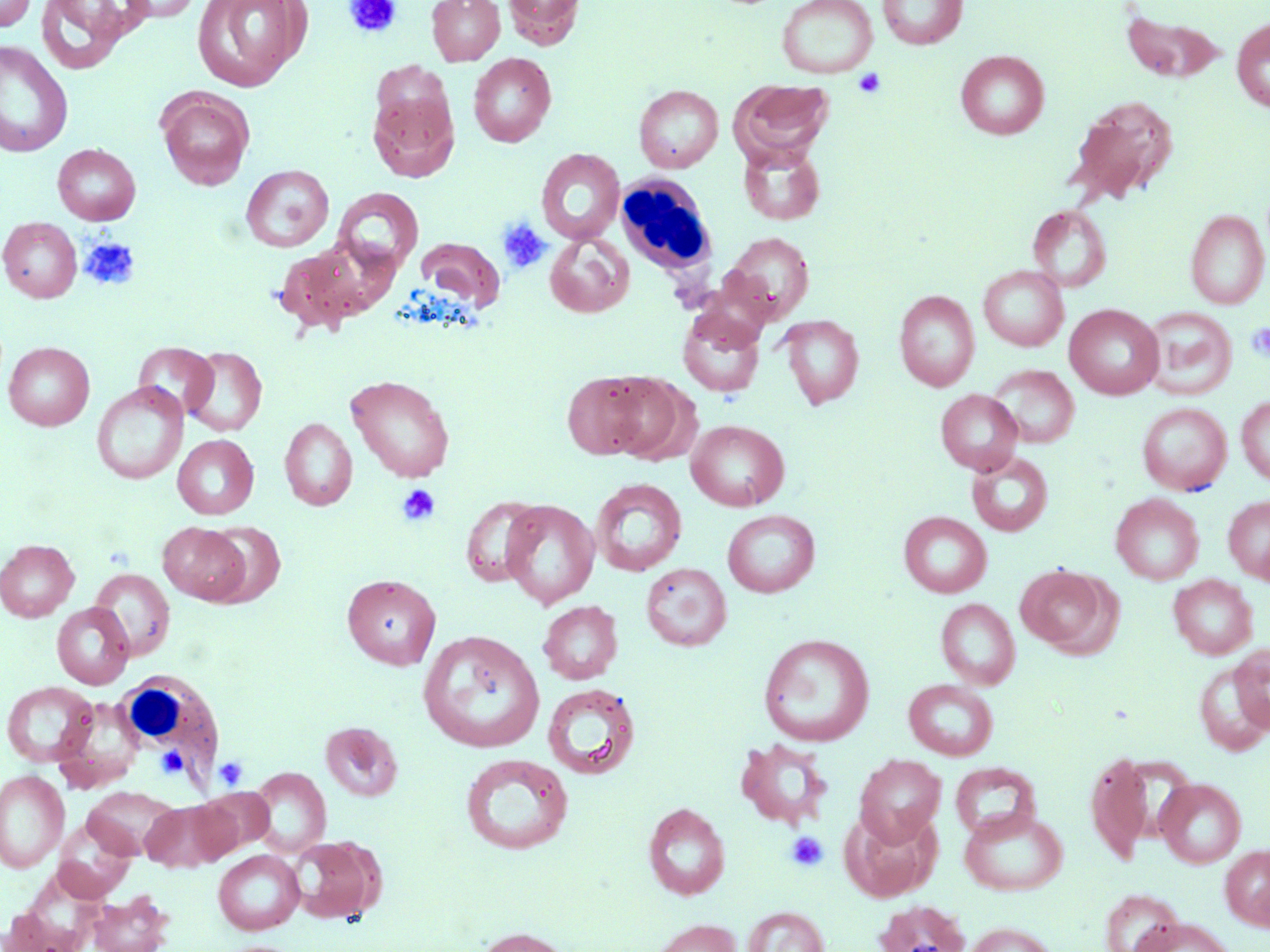

Summary:
  - Coordinate format: approximate bounding boxes as named x1/y1/x2/y2 corners in pixels
  - Uninfected red blood cell locations: (x1=0, y1=0, x2=36, y2=31), (x1=35, y1=0, x2=142, y2=75), (x1=118, y1=0, x2=204, y2=23), (x1=192, y1=0, x2=310, y2=91), (x1=427, y1=0, x2=505, y2=65), (x1=502, y1=0, x2=586, y2=49), (x1=777, y1=0, x2=877, y2=79), (x1=877, y1=0, x2=968, y2=49), (x1=1120, y1=9, x2=1228, y2=85), (x1=1231, y1=17, x2=1269, y2=113), (x1=0, y1=41, x2=73, y2=158), (x1=956, y1=50, x2=1049, y2=139), (x1=468, y1=52, x2=556, y2=147), (x1=732, y1=80, x2=832, y2=163), (x1=634, y1=85, x2=724, y2=173), (x1=156, y1=87, x2=255, y2=190), (x1=368, y1=88, x2=459, y2=182), (x1=1069, y1=95, x2=1179, y2=204), (x1=53, y1=143, x2=140, y2=225), (x1=739, y1=143, x2=826, y2=225), (x1=536, y1=148, x2=625, y2=245), (x1=241, y1=164, x2=334, y2=251), (x1=333, y1=188, x2=423, y2=274), (x1=1028, y1=205, x2=1111, y2=292), (x1=1185, y1=209, x2=1268, y2=309), (x1=1, y1=217, x2=82, y2=302), (x1=545, y1=232, x2=635, y2=318), (x1=722, y1=232, x2=814, y2=323), (x1=416, y1=237, x2=505, y2=312), (x1=272, y1=242, x2=376, y2=335), (x1=979, y1=266, x2=1068, y2=351), (x1=895, y1=290, x2=979, y2=391), (x1=1065, y1=304, x2=1164, y2=400), (x1=1141, y1=306, x2=1237, y2=401), (x1=677, y1=309, x2=766, y2=397), (x1=778, y1=315, x2=865, y2=410), (x1=3, y1=341, x2=95, y2=430), (x1=134, y1=342, x2=219, y2=419), (x1=182, y1=346, x2=267, y2=436), (x1=988, y1=365, x2=1080, y2=448), (x1=561, y1=372, x2=658, y2=461), (x1=598, y1=372, x2=692, y2=463), (x1=346, y1=374, x2=455, y2=482), (x1=92, y1=383, x2=188, y2=485), (x1=935, y1=389, x2=1023, y2=475), (x1=1236, y1=395, x2=1270, y2=486), (x1=1137, y1=402, x2=1232, y2=495), (x1=279, y1=418, x2=357, y2=511), (x1=686, y1=419, x2=790, y2=511), (x1=172, y1=434, x2=259, y2=519), (x1=966, y1=451, x2=1053, y2=536), (x1=591, y1=478, x2=687, y2=576), (x1=1110, y1=494, x2=1204, y2=584), (x1=460, y1=495, x2=545, y2=587), (x1=1223, y1=495, x2=1270, y2=583), (x1=500, y1=500, x2=600, y2=609), (x1=722, y1=510, x2=820, y2=598), (x1=899, y1=511, x2=992, y2=598), (x1=158, y1=521, x2=250, y2=605), (x1=205, y1=521, x2=286, y2=606), (x1=0, y1=539, x2=79, y2=622), (x1=640, y1=562, x2=732, y2=651), (x1=1015, y1=564, x2=1116, y2=656), (x1=90, y1=568, x2=175, y2=660), (x1=342, y1=574, x2=441, y2=670), (x1=1168, y1=575, x2=1257, y2=659), (x1=935, y1=598, x2=1020, y2=689), (x1=538, y1=600, x2=623, y2=684), (x1=52, y1=602, x2=134, y2=689), (x1=418, y1=630, x2=545, y2=753), (x1=758, y1=633, x2=875, y2=747), (x1=1230, y1=645, x2=1270, y2=733), (x1=1194, y1=659, x2=1270, y2=755), (x1=903, y1=679, x2=998, y2=761), (x1=2, y1=681, x2=99, y2=768), (x1=543, y1=683, x2=641, y2=780), (x1=54, y1=697, x2=144, y2=789), (x1=321, y1=722, x2=402, y2=801), (x1=734, y1=739, x2=833, y2=831), (x1=1086, y1=752, x2=1153, y2=863), (x1=460, y1=753, x2=574, y2=855), (x1=855, y1=754, x2=946, y2=845), (x1=950, y1=762, x2=1041, y2=841), (x1=250, y1=767, x2=331, y2=856), (x1=0, y1=769, x2=69, y2=873), (x1=1155, y1=778, x2=1246, y2=867), (x1=83, y1=786, x2=179, y2=859), (x1=194, y1=791, x2=273, y2=857), (x1=141, y1=800, x2=235, y2=872), (x1=643, y1=802, x2=730, y2=900), (x1=841, y1=807, x2=942, y2=902), (x1=959, y1=807, x2=1068, y2=896), (x1=53, y1=819, x2=134, y2=902), (x1=289, y1=835, x2=385, y2=924), (x1=1220, y1=844, x2=1270, y2=930), (x1=213, y1=850, x2=304, y2=934), (x1=1101, y1=889, x2=1184, y2=952), (x1=88, y1=890, x2=173, y2=952), (x1=872, y1=899, x2=972, y2=952), (x1=741, y1=906, x2=829, y2=952), (x1=1134, y1=917, x2=1237, y2=951), (x1=649, y1=918, x2=742, y2=952), (x1=963, y1=922, x2=1058, y2=952), (x1=474, y1=926, x2=574, y2=952)
  - Platelet locations: (x1=343, y1=0, x2=402, y2=39), (x1=853, y1=68, x2=886, y2=99), (x1=497, y1=217, x2=552, y2=274), (x1=79, y1=236, x2=140, y2=291), (x1=1245, y1=323, x2=1270, y2=362), (x1=396, y1=484, x2=440, y2=527), (x1=156, y1=746, x2=188, y2=778), (x1=214, y1=756, x2=248, y2=791), (x1=786, y1=831, x2=829, y2=871)
  - White blood cell locations: (x1=615, y1=176, x2=717, y2=278), (x1=116, y1=671, x2=223, y2=781)
  - Slide-level diagnosis: negative for blood parasites
  - Modality: light microscopy
  - Field of view: one of a larger specimen
  - Magnification: 1000x
  - Stain: May-Grünwald-Giemsa
  - Preparation: thin blood film
  - Image size: 1270×952 pixels